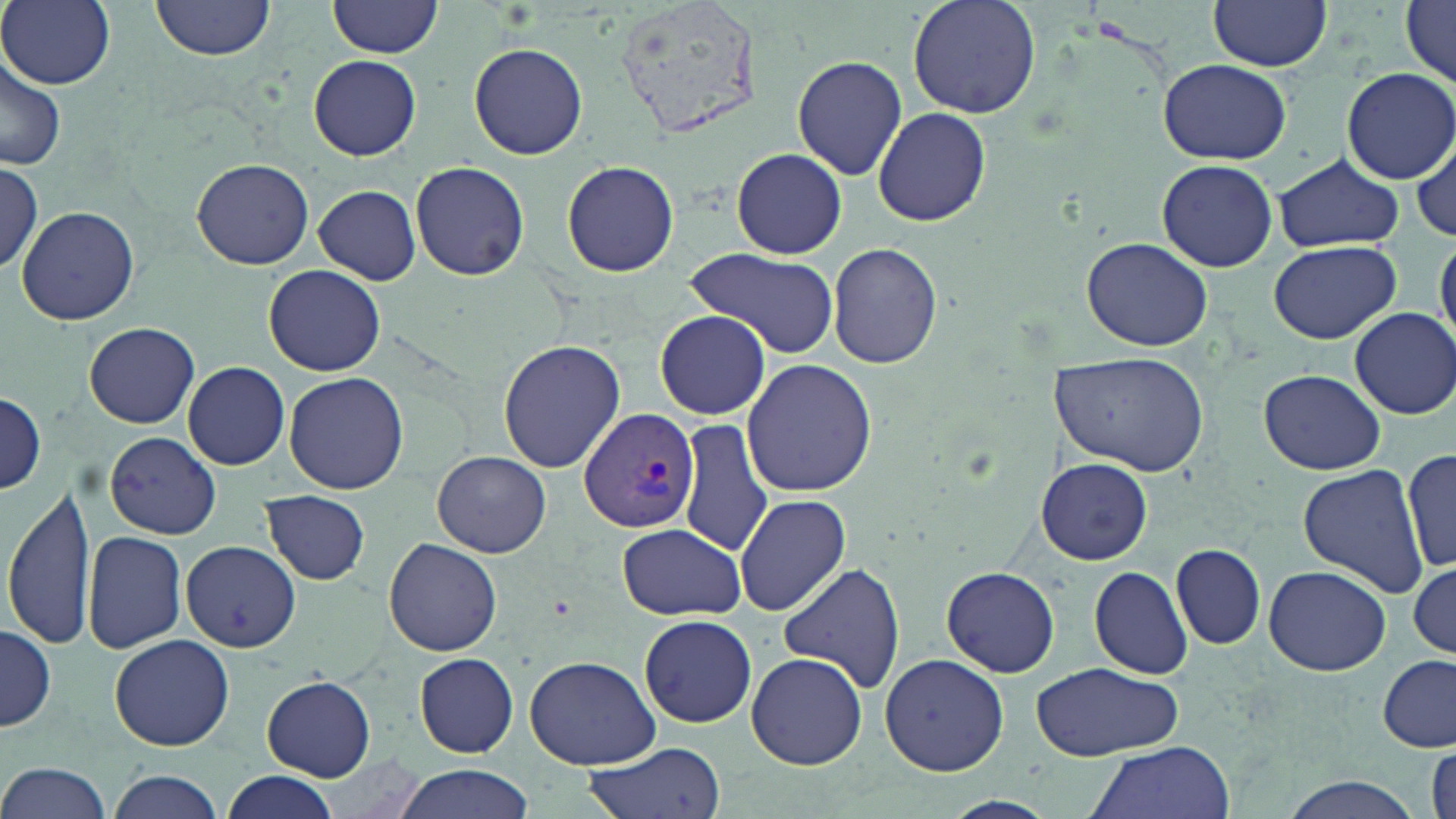
Approximate bounding boxes as (x1, y1, x2, y2) in pixels. Plasmodium vivax-infected red blood cell locations: (577, 406, 699, 536). Uninfected red blood cell locations: (2, 0, 115, 90), (151, 0, 275, 61), (329, 0, 442, 58), (909, 0, 1042, 117), (1208, 0, 1333, 71), (1400, 3, 1456, 86), (469, 42, 588, 160), (306, 55, 423, 161), (0, 56, 65, 170), (791, 56, 908, 180), (1159, 59, 1291, 164), (1338, 66, 1456, 184), (874, 106, 991, 227), (1412, 133, 1455, 246), (732, 148, 849, 258), (1273, 153, 1403, 252), (1, 156, 43, 275), (192, 158, 313, 270), (563, 160, 679, 278), (1157, 160, 1278, 271), (410, 161, 529, 281), (314, 185, 422, 285), (17, 206, 139, 326), (1434, 235, 1455, 350), (1081, 238, 1212, 350), (1269, 240, 1400, 344), (827, 242, 944, 368), (685, 250, 839, 359), (265, 265, 384, 377), (1347, 307, 1456, 419), (654, 310, 773, 418), (84, 322, 200, 427), (497, 339, 625, 472), (1051, 354, 1210, 472), (742, 360, 878, 499), (183, 361, 290, 469), (1260, 369, 1387, 475), (284, 371, 410, 495), (0, 390, 46, 496), (677, 419, 771, 556), (107, 432, 220, 538), (1402, 448, 1456, 576), (433, 450, 550, 558), (1038, 457, 1152, 565), (1297, 465, 1428, 597), (3, 482, 98, 652), (262, 491, 370, 584), (735, 493, 850, 617), (617, 523, 746, 621), (82, 529, 187, 653), (385, 538, 504, 657), (182, 541, 299, 651), (1172, 544, 1265, 649), (1410, 558, 1455, 663), (775, 562, 906, 695), (1088, 565, 1192, 680), (1265, 565, 1391, 675), (941, 566, 1061, 677), (638, 614, 758, 729), (1, 624, 55, 731), (111, 633, 234, 750), (746, 651, 869, 770), (879, 652, 1008, 776), (414, 653, 518, 757), (1376, 654, 1455, 755), (525, 655, 659, 769), (1030, 661, 1182, 762), (262, 675, 376, 779), (582, 739, 726, 819), (1083, 741, 1238, 819), (0, 762, 113, 819), (392, 763, 536, 819), (105, 770, 226, 818), (222, 772, 340, 819), (1279, 775, 1427, 819). Slide-level diagnosis: Plasmodium vivax. Light microscopy. Single field of view. Thin blood smear. 1000x magnification. Image is 1456×819 pixels. May-Grünwald-Giemsa-stained preparation.